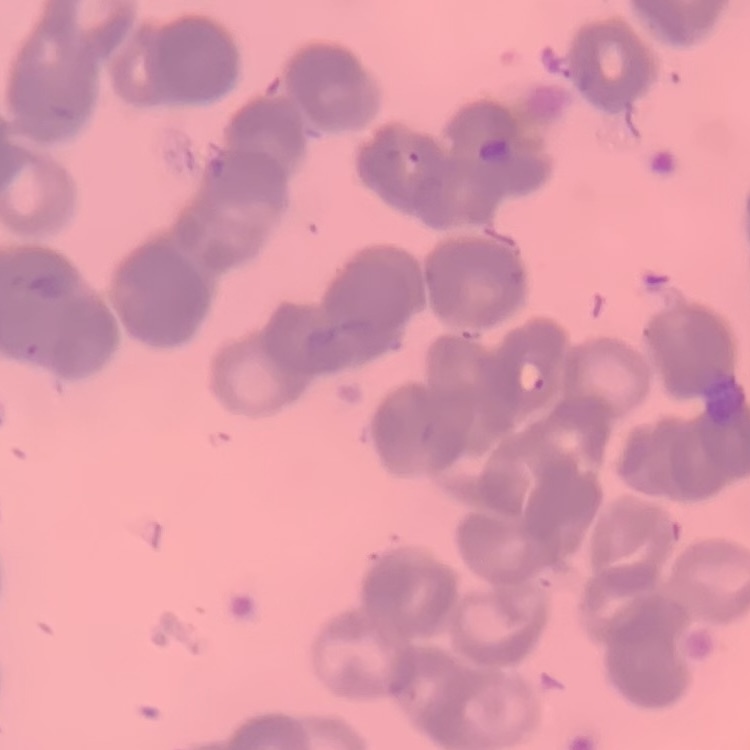
{
  "red_blood_cell_morphology": "rouleaux formation",
  "stain": "Field's or Giemsa",
  "preparation": "thin blood film",
  "image_type": "one tile cut from a larger photomicrograph"
}